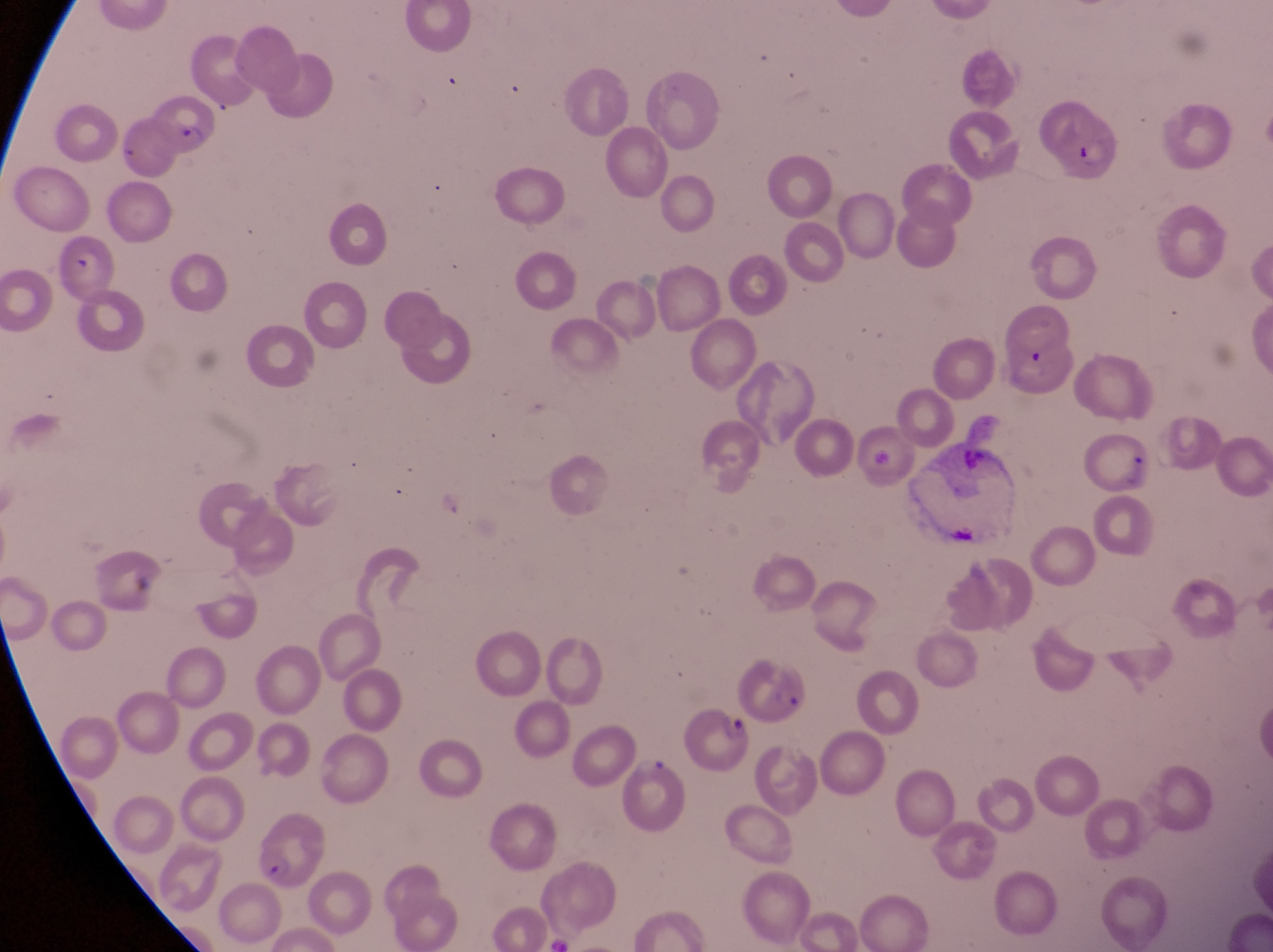 Approximate bounding boxes as (left, top, right, bottom) in pixels. Parasitised red blood cell locations: (150, 100, 222, 162), (1038, 100, 1118, 183), (684, 705, 756, 780), (626, 759, 695, 836), (250, 821, 322, 893). Artifact (platelet-like body, stain precipitate, or debris) locations: (60, 247, 92, 286), (1018, 345, 1060, 388). At a magnification of 1000x. Photographed through the eyepiece of an Olympus CX-23 microscope with a smartphone camera. Sample from Uganda. Thin blood smear. Single field of view. Image is 1273×952 pixels.